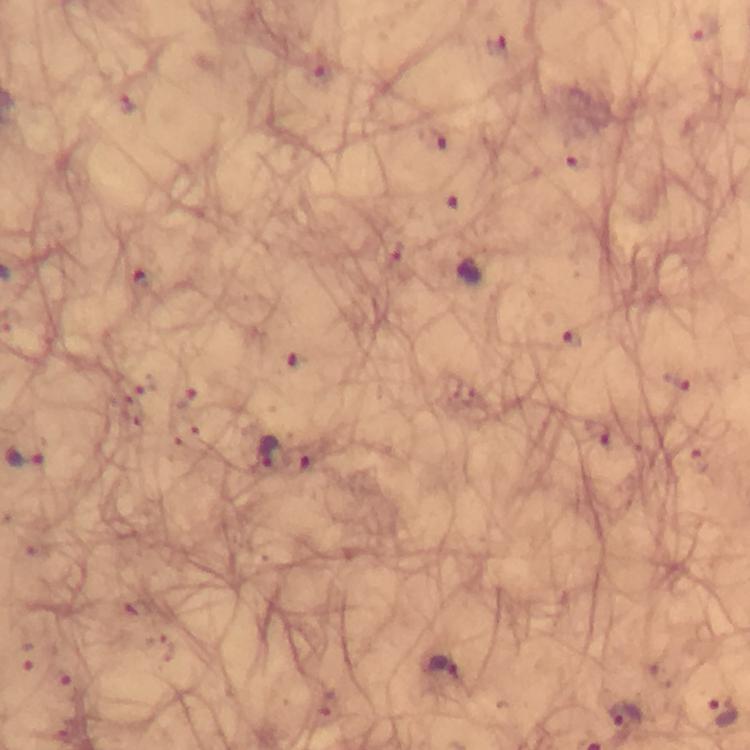
Approximate centers as {x, y} in pixels. Malaria parasite locations: {704, 30}, {498, 46}, {432, 138}, {579, 161}, {570, 339}, {679, 380}, {597, 433}, {268, 454}, {24, 457}, {440, 668}, {722, 712}, {624, 715}. From a diagnostic examination for malaria. Image is 750×750 pixels. Giemsa-stained preparation. Immersion oil was used. 100x magnification. Photographed with a smartphone mounted on the microscope. A crop from one field of view. Thick smear.